Give the extent of all uninfected red blood cells.
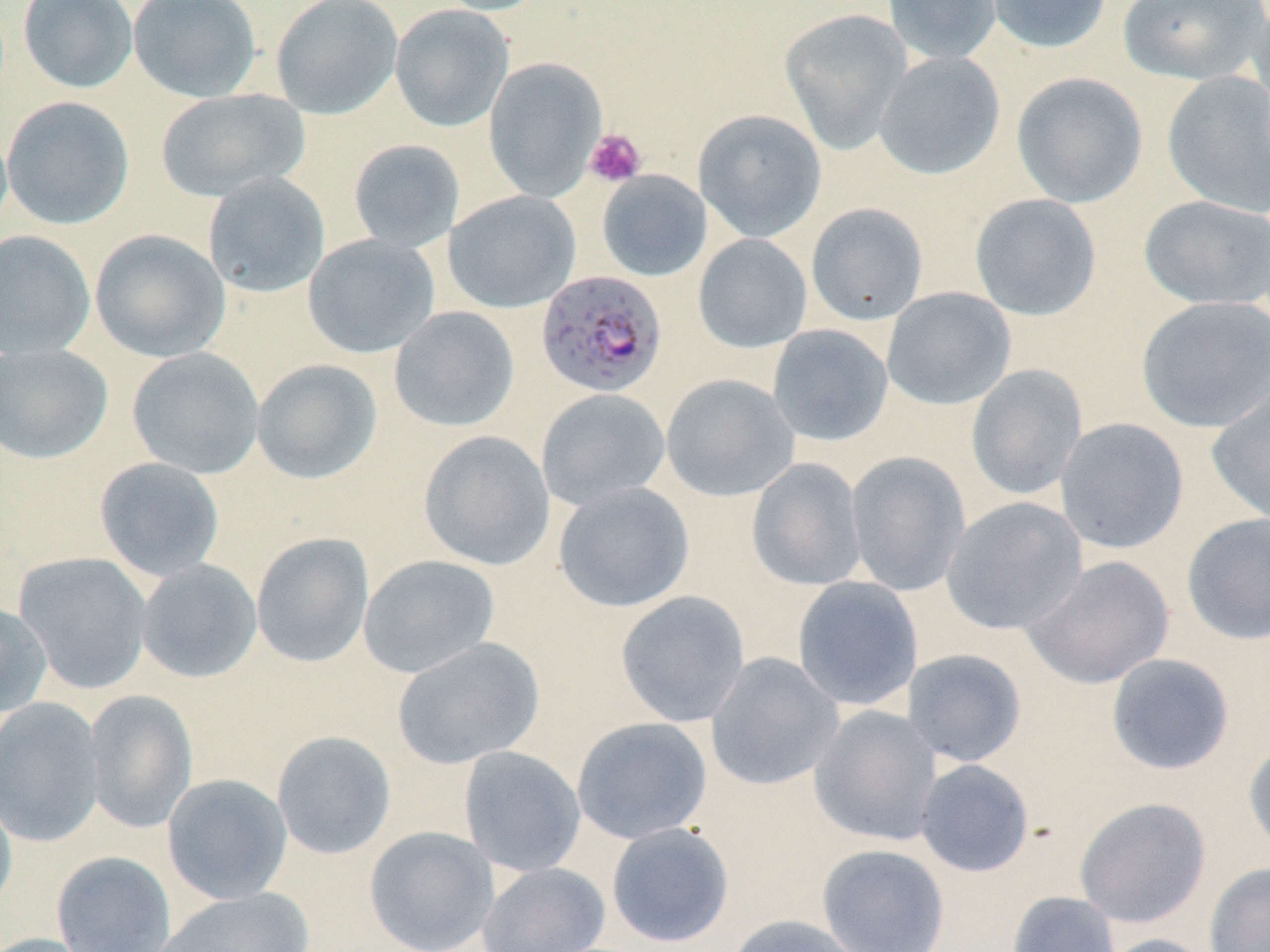

Approximate bounding boxes as [x1, y1, x2, y2] in pixels.
Uninfected red blood cells: [18, 0, 138, 94], [128, 0, 262, 103], [270, 0, 403, 120], [430, 0, 551, 16], [882, 0, 1002, 65], [983, 0, 1113, 54], [1117, 0, 1269, 85], [1247, 0, 1270, 120], [390, 4, 514, 132], [779, 8, 913, 154], [874, 51, 1005, 180], [483, 57, 607, 202], [1161, 71, 1270, 217], [1012, 72, 1148, 208], [155, 89, 309, 202], [1, 96, 134, 230], [693, 109, 827, 243], [0, 118, 13, 238], [347, 138, 465, 253], [597, 170, 712, 282], [202, 172, 330, 298], [443, 190, 581, 313], [969, 193, 1102, 321], [1138, 194, 1270, 311], [806, 203, 928, 326], [90, 229, 230, 362], [0, 230, 96, 361], [303, 234, 440, 358], [693, 234, 812, 353], [881, 287, 1016, 410], [1136, 296, 1270, 433], [389, 305, 520, 432], [767, 324, 894, 446], [0, 343, 114, 464], [127, 347, 264, 479], [251, 358, 382, 484], [966, 364, 1087, 501], [661, 373, 799, 502], [1206, 381, 1270, 526], [536, 388, 671, 511], [1055, 417, 1189, 555], [418, 430, 556, 571], [845, 451, 971, 596], [94, 457, 225, 582], [746, 457, 868, 591], [553, 482, 695, 613], [941, 496, 1087, 635], [1181, 512, 1270, 645], [251, 532, 374, 668], [14, 551, 153, 695], [358, 554, 501, 679], [1023, 555, 1174, 689], [135, 559, 263, 683], [792, 576, 923, 712], [615, 590, 750, 728], [0, 602, 52, 716], [392, 637, 544, 769], [902, 649, 1027, 767], [705, 652, 843, 792], [1105, 653, 1235, 775], [83, 689, 197, 834], [0, 697, 106, 847], [809, 705, 943, 846], [571, 716, 712, 844], [271, 730, 397, 860], [1244, 738, 1270, 857], [458, 746, 586, 878], [915, 759, 1035, 877], [162, 773, 293, 905], [0, 784, 18, 919], [1075, 797, 1210, 928], [606, 822, 734, 948], [363, 826, 499, 952], [816, 843, 950, 951], [51, 851, 176, 952], [477, 862, 611, 952], [1204, 862, 1270, 952], [156, 887, 316, 951], [1008, 890, 1120, 952], [722, 914, 868, 952], [0, 933, 98, 952], [1095, 933, 1216, 952].

{
  "slide_level_diagnosis": "Plasmodium falciparum",
  "stain": "May-Grünwald-Giemsa",
  "preparation": "thin blood smear",
  "modality": "light microscopy",
  "plasmodium_falciparum_infected_red_blood_cell_locations": "approximate bounding boxes as [x1, y1, x2, y2] in pixels: [536, 270, 668, 398]",
  "field_of_view": "one of a larger specimen",
  "platelet_locations": "approximate bounding boxes as [x1, y1, x2, y2] in pixels: [584, 128, 646, 187]",
  "magnification": "1000x",
  "image_size": "1270×952 pixels"
}